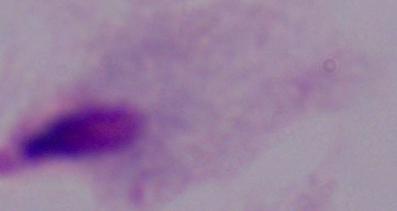

magnification = 1000x
identification = trichomonad
modality = photomicrograph